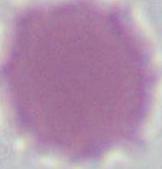

Summary:
  - Magnification: 1000x
  - Modality: micrograph
  - Identification: red blood cell